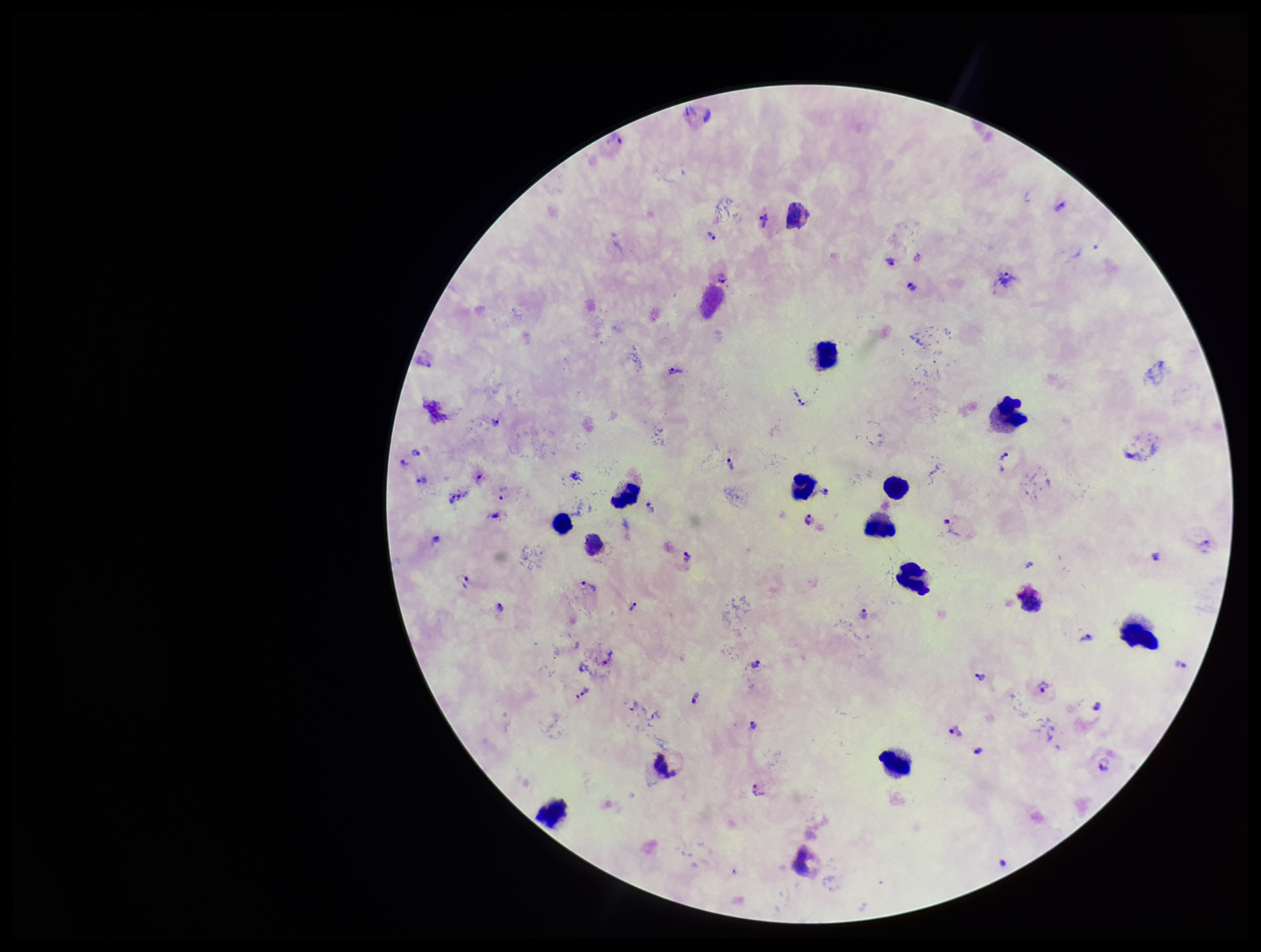
Summary:
  - Patient malaria status: positive
  - Species reported for this patient: Plasmodium vivax
  - Stain: Giemsa
  - Capture: smartphone photograph through the microscope eyepiece
  - Image size: 1261×952 pixels
  - Parasite count: 38
  - Preparation: thick
  - Plasmodium parasites: detected
  - Field of view: one from this slide
  - Leukocyte count: 14